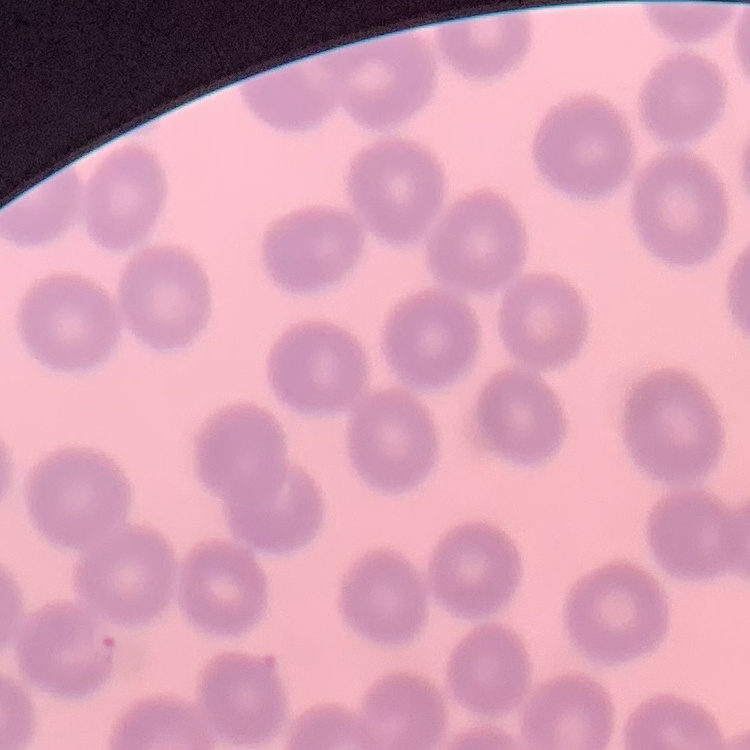

{
  "erythrocyte_morphology": "no rouleaux formation",
  "preparation": "thin peripheral smear",
  "stain": "Field's or Giemsa",
  "image_type": "one tile cut from a larger photomicrograph"
}